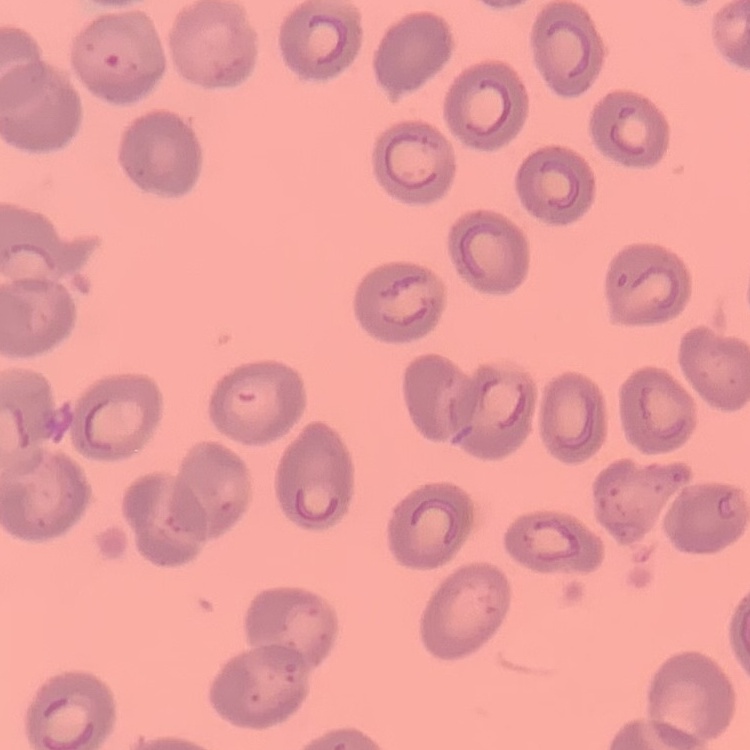
The red blood cells show no rouleaux formation. Thin blood smear. Field's or Giemsa stain. One tile cut from a larger photomicrograph.